Find each parasitized red blood cell.
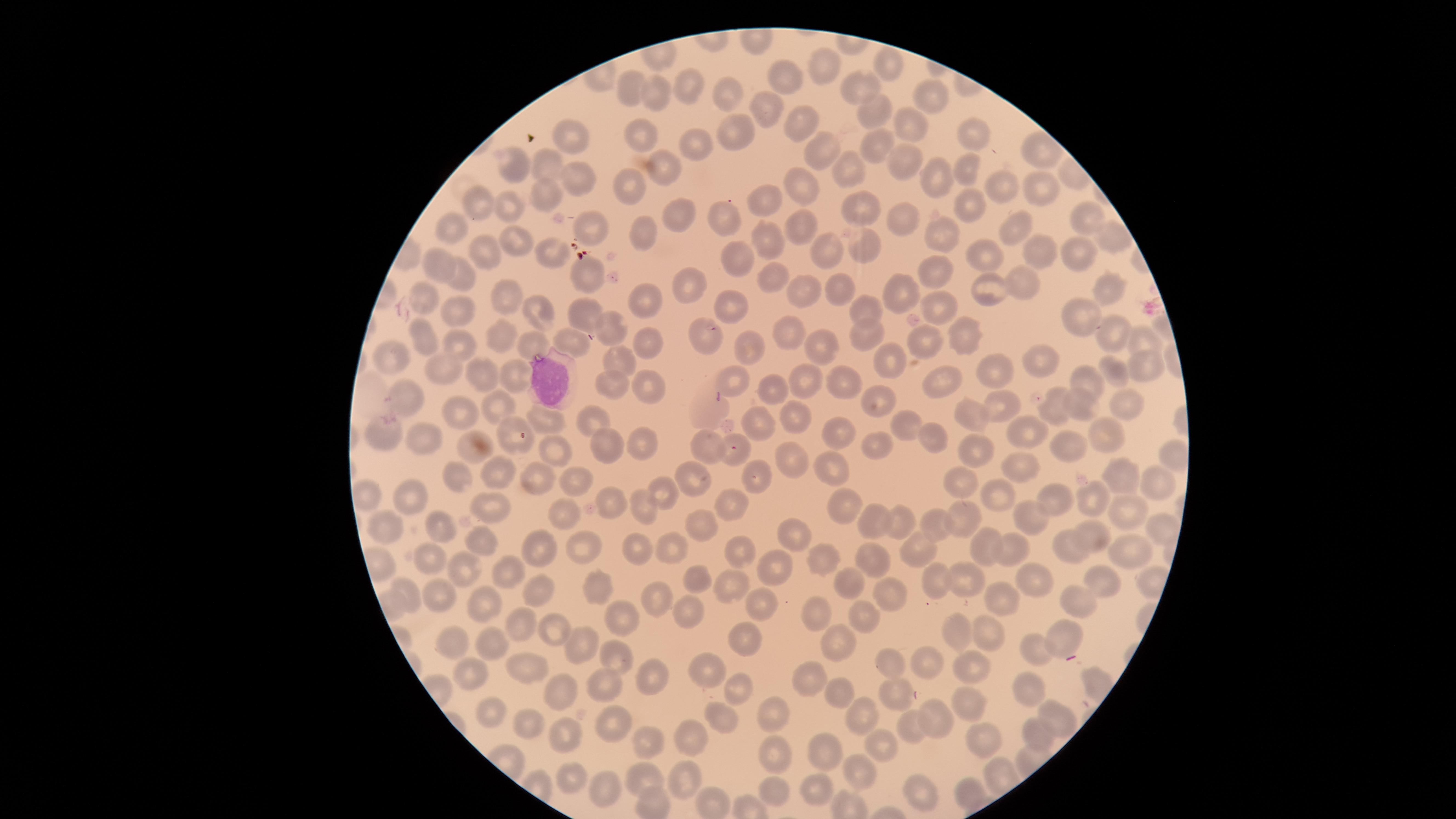

No parasitized red blood cells identified.

Approximate marker points as {x, y} in pixels. White blood cells: {554, 380}. Uninfected red blood cells: {888, 67}, {819, 69}, {788, 81}, {691, 85}, {858, 90}, {632, 92}, {658, 95}, {727, 97}, {926, 100}, {764, 111}, {870, 111}, {799, 122}, {908, 125}, {735, 131}, {972, 133}, {641, 136}, {575, 137}, {699, 144}, {875, 146}, {816, 154}, {513, 162}, {903, 164}, {544, 167}, {845, 170}, {968, 171}, {663, 174}, {573, 175}, {1034, 182}, {937, 184}, {630, 187}, {1001, 189}, {797, 190}, {542, 194}, {770, 202}, {969, 205}, {478, 208}, {507, 208}, {861, 209}, {672, 217}, {723, 218}, {1084, 220}, {902, 222}, {1015, 223}, {794, 224}, {587, 227}, {451, 231}, {643, 236}, {935, 236}, {765, 238}, {1104, 240}, {513, 241}, {1028, 249}, {861, 251}, {821, 252}, {545, 254}, {479, 255}, {1074, 256}, {984, 257}, {734, 259}, {441, 268}, {768, 273}, {943, 273}, {587, 274}, {464, 280}, {1020, 283}, {688, 287}, {837, 289}, {803, 291}, {989, 291}, {1109, 291}, {506, 295}, {902, 295}, {640, 298}, {421, 301}, {860, 308}, {724, 311}, {455, 312}, {539, 313}, {933, 313}, {582, 314}, {1077, 319}, {609, 324}, {961, 330}, {1106, 332}, {865, 334}, {706, 335}, {788, 335}, {420, 337}, {501, 337}, {1137, 338}, {458, 343}, {570, 344}, {649, 344}, {920, 344}, {745, 345}, {822, 345}, {529, 346}, {884, 358}, {1036, 360}, {392, 361}, {619, 363}, {1145, 367}, {444, 372}, {513, 375}, {1109, 375}, {480, 376}, {728, 376}, {988, 376}, {807, 380}, {1086, 385}, {610, 386}, {648, 386}, {771, 386}, {843, 386}, {938, 386}, {405, 396}, {884, 403}, {1004, 404}, {1121, 405}, {1085, 406}, {454, 407}, {497, 411}, {1052, 413}, {962, 414}, {706, 416}, {541, 419}, {595, 420}, {792, 421}, {764, 425}, {908, 426}, {508, 430}, {385, 438}, {927, 438}, {1029, 438}, {430, 439}, {839, 439}, {1106, 439}, {602, 442}, {640, 446}, {876, 447}, {1074, 447}, {471, 448}, {706, 449}, {555, 453}, {979, 453}, {732, 456}, {794, 462}, {1023, 468}, {492, 471}, {832, 472}, {691, 475}, {757, 476}, {1120, 476}, {535, 480}, {959, 481}, {458, 483}, {580, 483}, {1161, 483}, {665, 491}, {407, 493}, {997, 493}, {367, 497}, {1056, 498}, {1096, 499}, {488, 505}, {724, 505}, {846, 505}, {609, 506}, {644, 508}, {562, 514}, {1131, 515}, {699, 517}, {876, 518}, {1031, 518}, {964, 522}, {899, 523}, {939, 523}, {381, 528}, {1154, 532}, {445, 533}, {1096, 533}, {794, 534}, {481, 541}, {538, 545}, {1069, 547}, {591, 548}, {639, 548}, {1008, 548}, {986, 549}, {674, 551}, {920, 551}, {1128, 551}, {735, 552}, {820, 555}, {431, 560}, {876, 562}, {505, 570}, {458, 571}, {772, 574}, {691, 578}, {963, 578}, {933, 579}, {851, 580}, {1103, 581}, {1038, 586}, {534, 588}, {438, 590}, {724, 590}, {594, 592}, {888, 594}, {998, 595}, {656, 598}, {1081, 601}, {486, 605}, {761, 606}, {682, 611}, {617, 614}, {809, 614}, {863, 616}, {522, 623}, {551, 631}, {990, 633}, {1062, 635}, {954, 636}, {450, 637}, {750, 638}, {577, 641}, {835, 642}, {487, 643}, {1036, 647}, {613, 654}, {924, 660}, {889, 664}, {527, 665}, {699, 668}, {975, 668}, {468, 670}, {656, 679}, {808, 679}, {1029, 686}, {740, 688}, {608, 689}, {838, 693}, {560, 695}, {897, 695}, {967, 699}, {489, 712}, {859, 714}, {722, 715}, {774, 715}, {938, 722}, {1050, 722}, {608, 723}, {914, 725}, {530, 729}, {692, 733}, {563, 735}, {1031, 737}, {983, 738}, {880, 740}, {648, 745}, {820, 749}, {778, 757}, {861, 771}, {683, 778}, {572, 779}, {642, 781}, {603, 786}, {819, 789}, {769, 791}, {919, 792}, {966, 794}. The visible region is circular. Giemsa-stained preparation. One field of view of the specimen. Thin blood film. Photographed with a smartphone camera through the microscope eyepiece. Image is 1456×819 pixels.